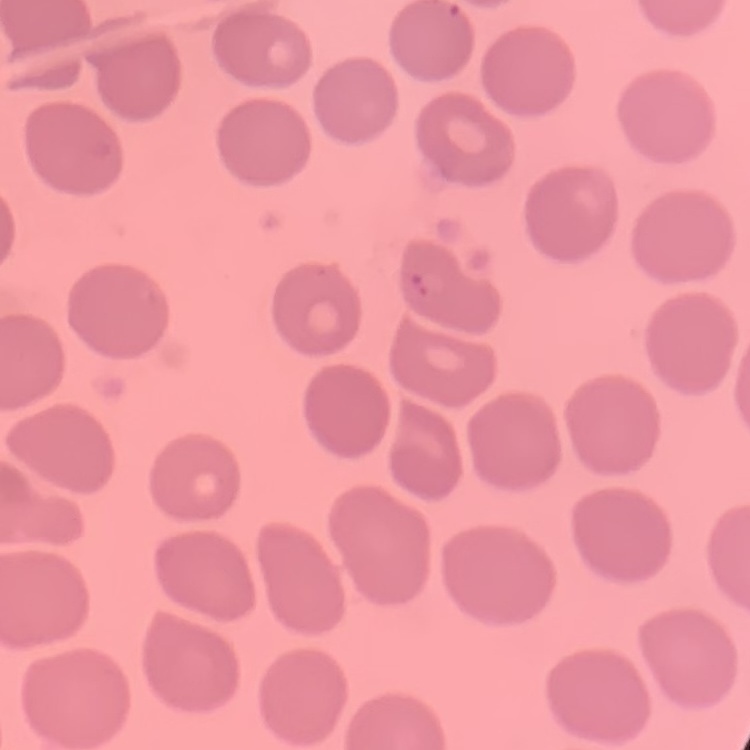

{
  "red_blood_cell_morphology": "no rouleaux formation",
  "image_type": "one tile cut from a larger photomicrograph",
  "preparation": "thin peripheral smear",
  "stain": "Field's or Giemsa"
}